State which cell type is depicted.
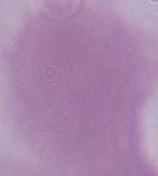
This is an erythrocyte.

magnification = 1000x
modality = micrograph